Point out each Plasmodium parasite.
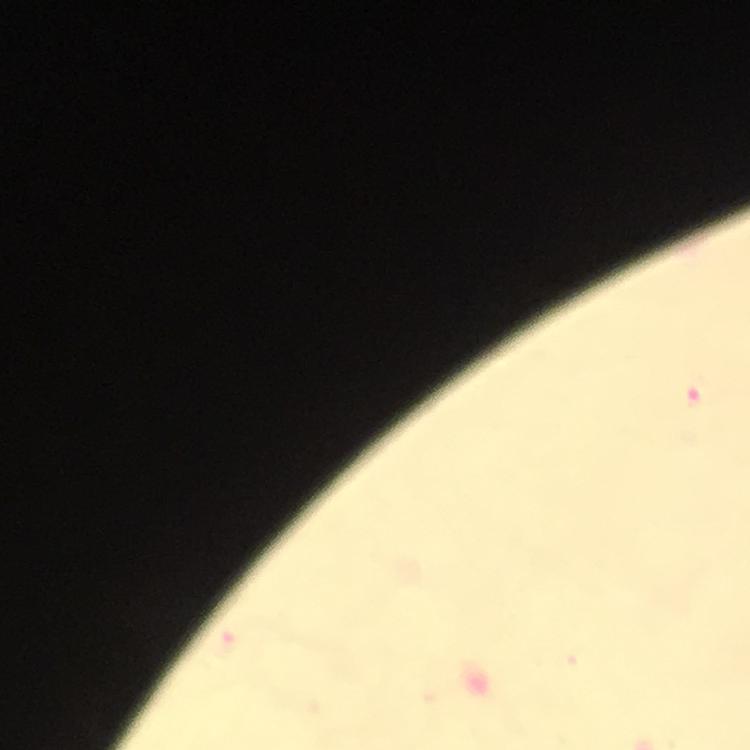

Approximate object centers, in pixels from the top-left corner.
Plasmodium parasites: (x=693, y=399).

Summary:
  - Stain: Giemsa
  - Context: from a diagnostic examination for malaria
  - Preparation: thick blood film
  - Cropped from: one field of view
  - Image size: 750×750 pixels
  - Immersion oil: applied
  - Capture: smartphone camera through the microscope
  - Magnification: 100x